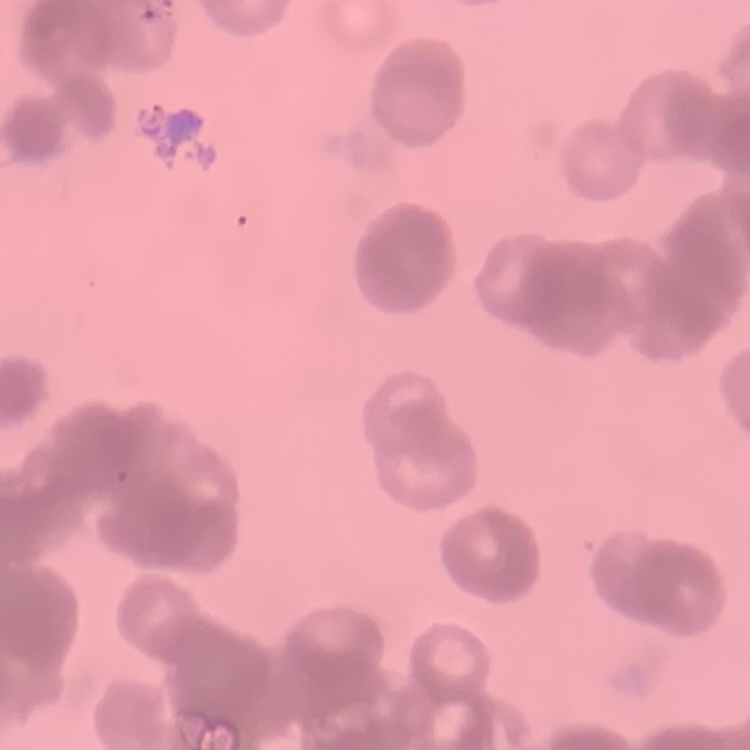

red blood cell morphology = rouleaux formation
stain = Field's or Giemsa
preparation = thin peripheral smear
image type = square crop of a larger photomicrograph